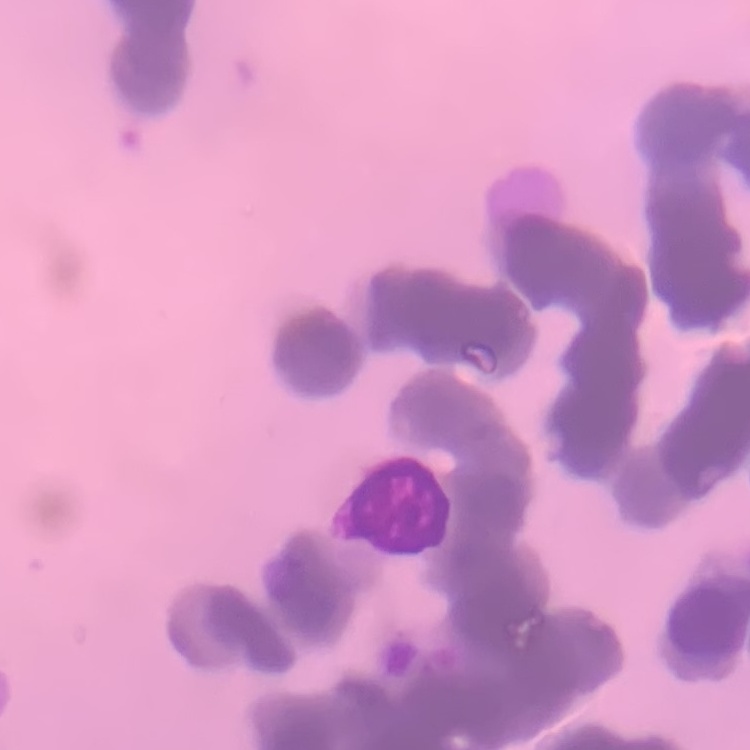

Summary:
  - Erythrocyte morphology: rouleaux formation
  - Preparation: thin blood film
  - Stain: Field's or Giemsa
  - Image type: square crop of a larger photomicrograph